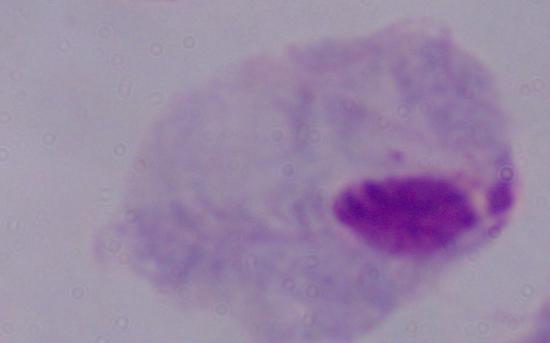

magnification = 1000x
modality = micrograph
identification = trichomonad